Locate and identify every blood parasite.
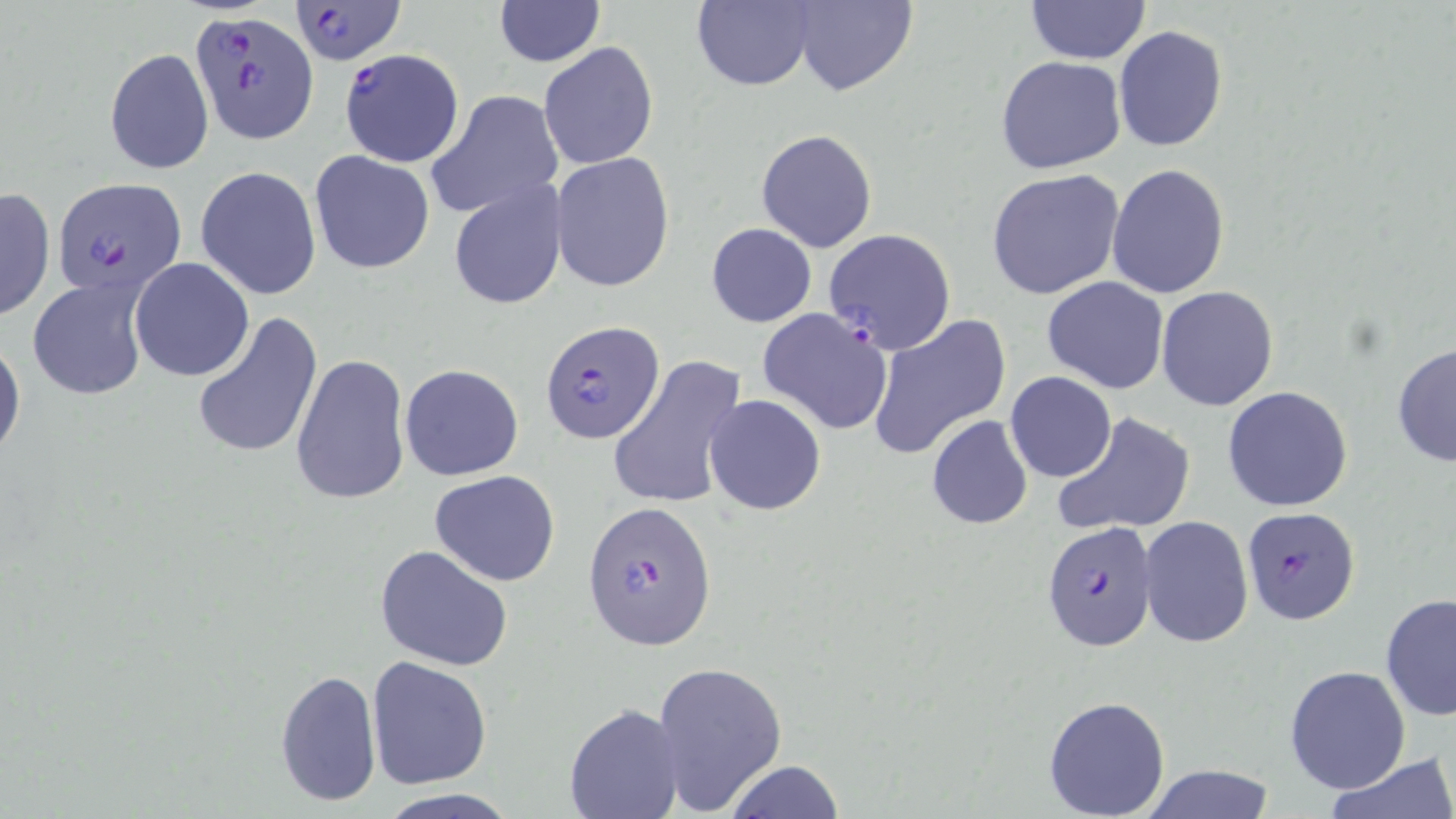
Approximate bounding boxes as named x1/y1/x2/y2 corners in pixels.
Plasmodium falciparum-infected red blood cells: (x1=293, y1=1, x2=404, y2=66), (x1=188, y1=11, x2=320, y2=144), (x1=338, y1=48, x2=465, y2=168), (x1=51, y1=176, x2=186, y2=301), (x1=824, y1=229, x2=955, y2=354), (x1=539, y1=320, x2=663, y2=446), (x1=583, y1=502, x2=717, y2=650), (x1=1241, y1=507, x2=1362, y2=626), (x1=1041, y1=519, x2=1157, y2=651).
No Plasmodium ovale, Plasmodium malariae, Plasmodium vivax, Babesia divergens, or Trypanosoma brucei observed.

Summary:
  - Uninfected red blood cell locations: (x1=793, y1=0, x2=917, y2=97), (x1=1026, y1=0, x2=1150, y2=65), (x1=493, y1=1, x2=605, y2=66), (x1=693, y1=1, x2=817, y2=91), (x1=1113, y1=25, x2=1228, y2=152), (x1=537, y1=42, x2=659, y2=172), (x1=104, y1=46, x2=213, y2=174), (x1=995, y1=55, x2=1126, y2=174), (x1=425, y1=90, x2=565, y2=220), (x1=756, y1=129, x2=877, y2=252), (x1=309, y1=151, x2=435, y2=275), (x1=551, y1=153, x2=675, y2=293), (x1=1106, y1=163, x2=1231, y2=300), (x1=195, y1=165, x2=322, y2=302), (x1=986, y1=168, x2=1128, y2=302), (x1=448, y1=179, x2=568, y2=311), (x1=0, y1=186, x2=55, y2=324), (x1=705, y1=222, x2=817, y2=328), (x1=129, y1=258, x2=254, y2=380), (x1=1041, y1=276, x2=1168, y2=393), (x1=27, y1=278, x2=147, y2=399), (x1=1156, y1=285, x2=1278, y2=411), (x1=757, y1=307, x2=895, y2=435), (x1=190, y1=309, x2=324, y2=462), (x1=866, y1=314, x2=1012, y2=460), (x1=0, y1=331, x2=26, y2=466), (x1=1391, y1=341, x2=1456, y2=469), (x1=291, y1=354, x2=412, y2=507), (x1=611, y1=357, x2=750, y2=513), (x1=399, y1=363, x2=524, y2=482), (x1=1005, y1=371, x2=1116, y2=482), (x1=1222, y1=385, x2=1353, y2=512), (x1=703, y1=394, x2=827, y2=516), (x1=1050, y1=411, x2=1196, y2=537), (x1=925, y1=414, x2=1033, y2=530), (x1=430, y1=470, x2=560, y2=586), (x1=1139, y1=514, x2=1253, y2=650), (x1=374, y1=545, x2=513, y2=669), (x1=1380, y1=593, x2=1456, y2=721), (x1=367, y1=657, x2=493, y2=790), (x1=651, y1=659, x2=788, y2=816), (x1=1283, y1=665, x2=1412, y2=795), (x1=274, y1=667, x2=382, y2=808), (x1=1043, y1=695, x2=1170, y2=817), (x1=564, y1=703, x2=684, y2=819), (x1=1326, y1=755, x2=1456, y2=818), (x1=721, y1=762, x2=844, y2=819), (x1=1138, y1=764, x2=1277, y2=819), (x1=376, y1=790, x2=516, y2=819)
  - Slide-level diagnosis: Plasmodium falciparum
  - Modality: optical microscopy
  - Preparation: thin blood smear
  - Field of view: single
  - Stain: May-Grünwald-Giemsa
  - Magnification: 1000x
  - Image size: 1456×819 pixels